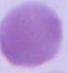

magnification = 1000x
identification = erythrocyte
modality = micrograph